Give the extent of all Plasmodium ovale-infected red blood cells.
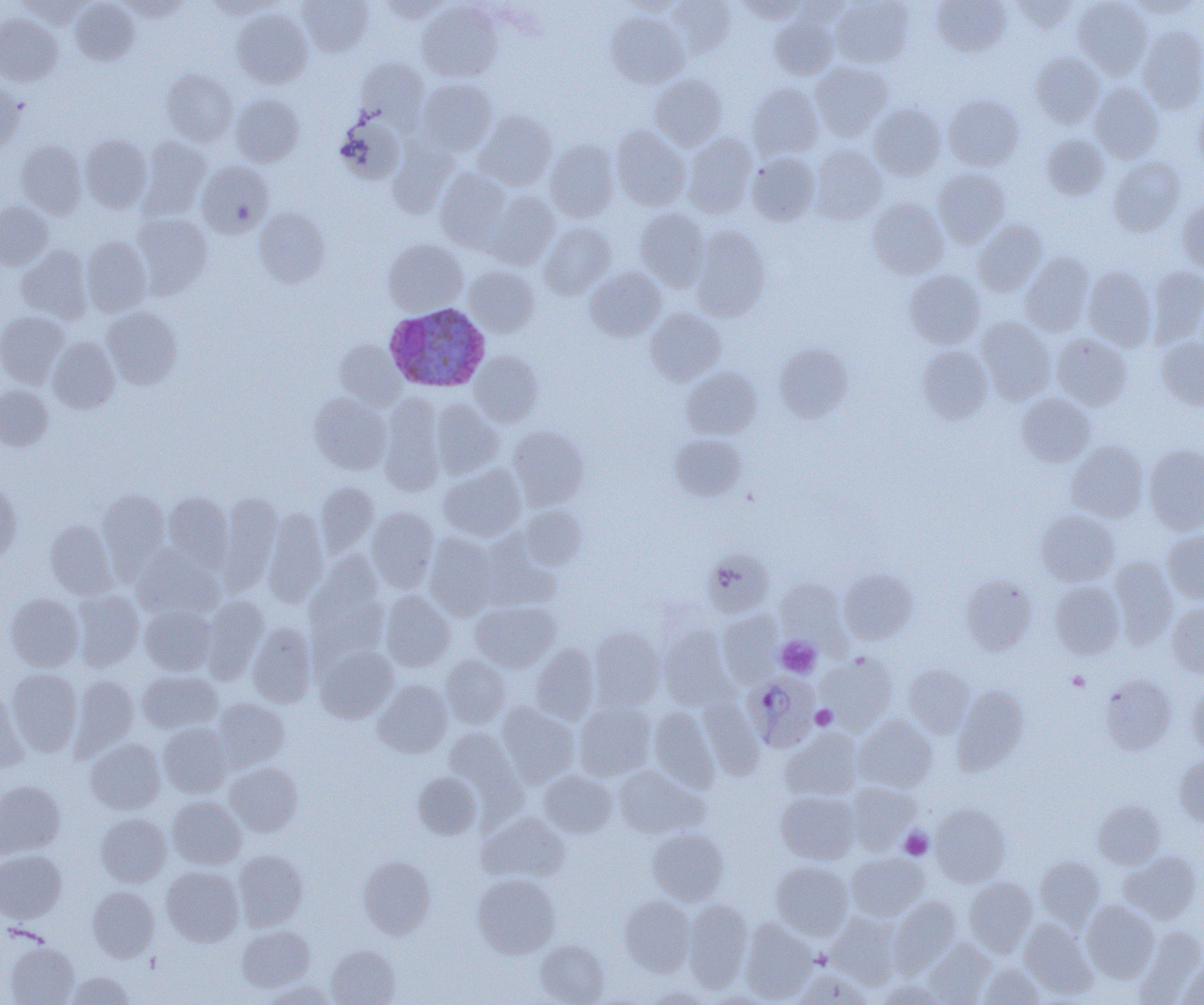

Approximate bounding boxes as named x1/y1/x2/y2 corners in pixels.
Plasmodium ovale-infected red blood cells: (x1=383, y1=303, x2=490, y2=392), (x1=746, y1=673, x2=820, y2=751).

slide-level diagnosis = Plasmodium ovale
magnification = 1000x
platelet locations = approximate bounding boxes as named x1/y1/x2/y2 corners in pixels: (x1=776, y1=636, x2=821, y2=678), (x1=1067, y1=671, x2=1089, y2=690), (x1=811, y1=705, x2=837, y2=729), (x1=899, y1=828, x2=933, y2=859)
field of view = one of a larger specimen
modality = optical microscopy
image size = 1204×1005 pixels
preparation = thin blood film
uninfected red blood cell locations = approximate bounding boxes as named x1/y1/x2/y2 corners in pixels: (x1=70, y1=0, x2=140, y2=65), (x1=119, y1=0, x2=192, y2=20), (x1=297, y1=0, x2=374, y2=56), (x1=621, y1=0, x2=688, y2=17), (x1=669, y1=0, x2=736, y2=55), (x1=738, y1=0, x2=810, y2=23), (x1=831, y1=0, x2=913, y2=68), (x1=931, y1=0, x2=1011, y2=56), (x1=1073, y1=0, x2=1152, y2=79), (x1=1129, y1=0, x2=1201, y2=20), (x1=17, y1=1, x2=90, y2=27), (x1=204, y1=1, x2=280, y2=19), (x1=377, y1=1, x2=450, y2=24), (x1=417, y1=1, x2=503, y2=82), (x1=1011, y1=1, x2=1079, y2=33), (x1=232, y1=9, x2=312, y2=88), (x1=606, y1=12, x2=689, y2=87), (x1=0, y1=14, x2=63, y2=85), (x1=769, y1=15, x2=838, y2=80), (x1=1137, y1=26, x2=1204, y2=114), (x1=1030, y1=52, x2=1104, y2=126), (x1=356, y1=58, x2=428, y2=127), (x1=810, y1=61, x2=894, y2=140), (x1=161, y1=69, x2=237, y2=145), (x1=650, y1=75, x2=727, y2=151), (x1=416, y1=79, x2=497, y2=155), (x1=0, y1=82, x2=25, y2=153), (x1=748, y1=83, x2=823, y2=159), (x1=1089, y1=83, x2=1163, y2=162), (x1=230, y1=93, x2=304, y2=167), (x1=944, y1=94, x2=1024, y2=170), (x1=1193, y1=97, x2=1204, y2=172), (x1=868, y1=104, x2=946, y2=180), (x1=475, y1=112, x2=557, y2=190), (x1=336, y1=114, x2=405, y2=184), (x1=611, y1=125, x2=691, y2=211), (x1=683, y1=134, x2=756, y2=218), (x1=81, y1=135, x2=152, y2=212), (x1=1042, y1=135, x2=1109, y2=200), (x1=140, y1=137, x2=210, y2=216), (x1=388, y1=139, x2=459, y2=217), (x1=545, y1=139, x2=620, y2=222), (x1=16, y1=140, x2=87, y2=219), (x1=809, y1=145, x2=887, y2=224), (x1=747, y1=151, x2=820, y2=225), (x1=1108, y1=157, x2=1185, y2=235), (x1=197, y1=161, x2=273, y2=237), (x1=435, y1=168, x2=512, y2=252), (x1=933, y1=168, x2=1011, y2=248), (x1=486, y1=191, x2=558, y2=269), (x1=867, y1=197, x2=948, y2=279), (x1=1177, y1=198, x2=1204, y2=275), (x1=0, y1=202, x2=53, y2=269), (x1=255, y1=208, x2=330, y2=286), (x1=635, y1=208, x2=709, y2=290), (x1=132, y1=213, x2=212, y2=297), (x1=973, y1=220, x2=1048, y2=295), (x1=539, y1=223, x2=615, y2=298), (x1=691, y1=227, x2=771, y2=320), (x1=81, y1=237, x2=152, y2=316), (x1=383, y1=239, x2=467, y2=315), (x1=17, y1=245, x2=93, y2=323), (x1=1020, y1=252, x2=1095, y2=336), (x1=1083, y1=265, x2=1156, y2=350), (x1=464, y1=266, x2=540, y2=337), (x1=1147, y1=266, x2=1204, y2=345), (x1=585, y1=267, x2=667, y2=341), (x1=905, y1=269, x2=985, y2=348), (x1=102, y1=307, x2=182, y2=389), (x1=645, y1=308, x2=726, y2=384), (x1=0, y1=311, x2=70, y2=387), (x1=977, y1=317, x2=1056, y2=404), (x1=1052, y1=333, x2=1132, y2=409), (x1=47, y1=337, x2=119, y2=413), (x1=1157, y1=337, x2=1204, y2=410), (x1=335, y1=340, x2=405, y2=409), (x1=775, y1=344, x2=852, y2=421), (x1=917, y1=345, x2=992, y2=423), (x1=470, y1=351, x2=543, y2=426), (x1=681, y1=367, x2=762, y2=439), (x1=0, y1=384, x2=54, y2=450), (x1=309, y1=392, x2=391, y2=474), (x1=1016, y1=393, x2=1095, y2=466), (x1=379, y1=396, x2=445, y2=495), (x1=431, y1=399, x2=503, y2=478), (x1=508, y1=426, x2=589, y2=509), (x1=669, y1=434, x2=746, y2=501), (x1=1067, y1=441, x2=1148, y2=522), (x1=1144, y1=444, x2=1204, y2=534), (x1=439, y1=465, x2=526, y2=541), (x1=0, y1=481, x2=21, y2=564), (x1=315, y1=483, x2=378, y2=555), (x1=98, y1=489, x2=170, y2=568), (x1=163, y1=492, x2=233, y2=568), (x1=218, y1=494, x2=282, y2=592), (x1=518, y1=506, x2=587, y2=570), (x1=367, y1=507, x2=439, y2=591), (x1=262, y1=508, x2=328, y2=607), (x1=1036, y1=510, x2=1119, y2=586), (x1=44, y1=519, x2=118, y2=599), (x1=1163, y1=530, x2=1204, y2=603), (x1=424, y1=533, x2=499, y2=618), (x1=134, y1=548, x2=223, y2=619), (x1=703, y1=550, x2=774, y2=617), (x1=1109, y1=557, x2=1178, y2=648), (x1=304, y1=560, x2=388, y2=661), (x1=838, y1=568, x2=918, y2=644), (x1=960, y1=574, x2=1037, y2=654), (x1=776, y1=577, x2=848, y2=644), (x1=1050, y1=582, x2=1124, y2=658), (x1=72, y1=590, x2=144, y2=671), (x1=381, y1=591, x2=455, y2=671), (x1=5, y1=593, x2=83, y2=671), (x1=201, y1=595, x2=269, y2=684), (x1=471, y1=601, x2=559, y2=672), (x1=1167, y1=603, x2=1204, y2=678), (x1=140, y1=605, x2=216, y2=675), (x1=718, y1=611, x2=783, y2=686), (x1=248, y1=623, x2=317, y2=707), (x1=658, y1=625, x2=737, y2=711), (x1=589, y1=627, x2=665, y2=710), (x1=531, y1=644, x2=599, y2=724), (x1=315, y1=645, x2=398, y2=722), (x1=816, y1=652, x2=898, y2=733), (x1=441, y1=655, x2=510, y2=727), (x1=904, y1=663, x2=974, y2=736), (x1=6, y1=669, x2=83, y2=756), (x1=138, y1=671, x2=222, y2=734), (x1=71, y1=675, x2=139, y2=755), (x1=1100, y1=675, x2=1176, y2=754), (x1=373, y1=680, x2=452, y2=757), (x1=1187, y1=682, x2=1204, y2=756), (x1=952, y1=686, x2=1028, y2=774), (x1=0, y1=689, x2=28, y2=773), (x1=212, y1=698, x2=289, y2=771), (x1=698, y1=698, x2=764, y2=779), (x1=575, y1=701, x2=655, y2=780), (x1=498, y1=704, x2=579, y2=787), (x1=649, y1=706, x2=720, y2=791), (x1=854, y1=715, x2=937, y2=793), (x1=159, y1=723, x2=233, y2=797), (x1=443, y1=726, x2=523, y2=805), (x1=781, y1=729, x2=862, y2=802), (x1=85, y1=738, x2=165, y2=814), (x1=1174, y1=756, x2=1204, y2=826), (x1=225, y1=762, x2=303, y2=836), (x1=613, y1=766, x2=704, y2=839), (x1=539, y1=770, x2=618, y2=838), (x1=413, y1=772, x2=482, y2=839), (x1=0, y1=780, x2=65, y2=857), (x1=845, y1=781, x2=921, y2=852), (x1=776, y1=790, x2=860, y2=864), (x1=167, y1=796, x2=246, y2=868), (x1=1093, y1=801, x2=1165, y2=869), (x1=930, y1=804, x2=1011, y2=886), (x1=479, y1=812, x2=570, y2=884), (x1=96, y1=813, x2=171, y2=887), (x1=647, y1=827, x2=729, y2=905), (x1=0, y1=849, x2=66, y2=923), (x1=233, y1=850, x2=308, y2=931), (x1=1120, y1=851, x2=1201, y2=923), (x1=846, y1=852, x2=929, y2=920), (x1=358, y1=857, x2=436, y2=938), (x1=1035, y1=857, x2=1105, y2=929), (x1=771, y1=861, x2=853, y2=939), (x1=161, y1=866, x2=244, y2=945), (x1=472, y1=873, x2=561, y2=958), (x1=964, y1=877, x2=1037, y2=956), (x1=87, y1=886, x2=159, y2=962), (x1=619, y1=895, x2=695, y2=976), (x1=890, y1=897, x2=961, y2=974), (x1=683, y1=900, x2=752, y2=990), (x1=1082, y1=900, x2=1159, y2=982), (x1=828, y1=912, x2=902, y2=988), (x1=1019, y1=918, x2=1097, y2=998), (x1=739, y1=920, x2=816, y2=1003), (x1=237, y1=925, x2=315, y2=992), (x1=1136, y1=927, x2=1204, y2=1002), (x1=925, y1=938, x2=996, y2=1004), (x1=535, y1=940, x2=609, y2=1004), (x1=5, y1=941, x2=79, y2=1005), (x1=326, y1=945, x2=400, y2=1005), (x1=1178, y1=960, x2=1204, y2=1005), (x1=979, y1=963, x2=1043, y2=1004), (x1=793, y1=969, x2=872, y2=1005), (x1=65, y1=971, x2=136, y2=1004), (x1=262, y1=980, x2=338, y2=1005), (x1=876, y1=980, x2=947, y2=1005), (x1=645, y1=985, x2=712, y2=1004)